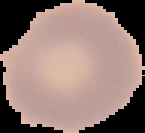
Summary:
  - Image size: 145×133 pixels
  - Image type: segmented cell region on a black background
  - Preparation: thin blood smear
  - Malaria status: uninfected